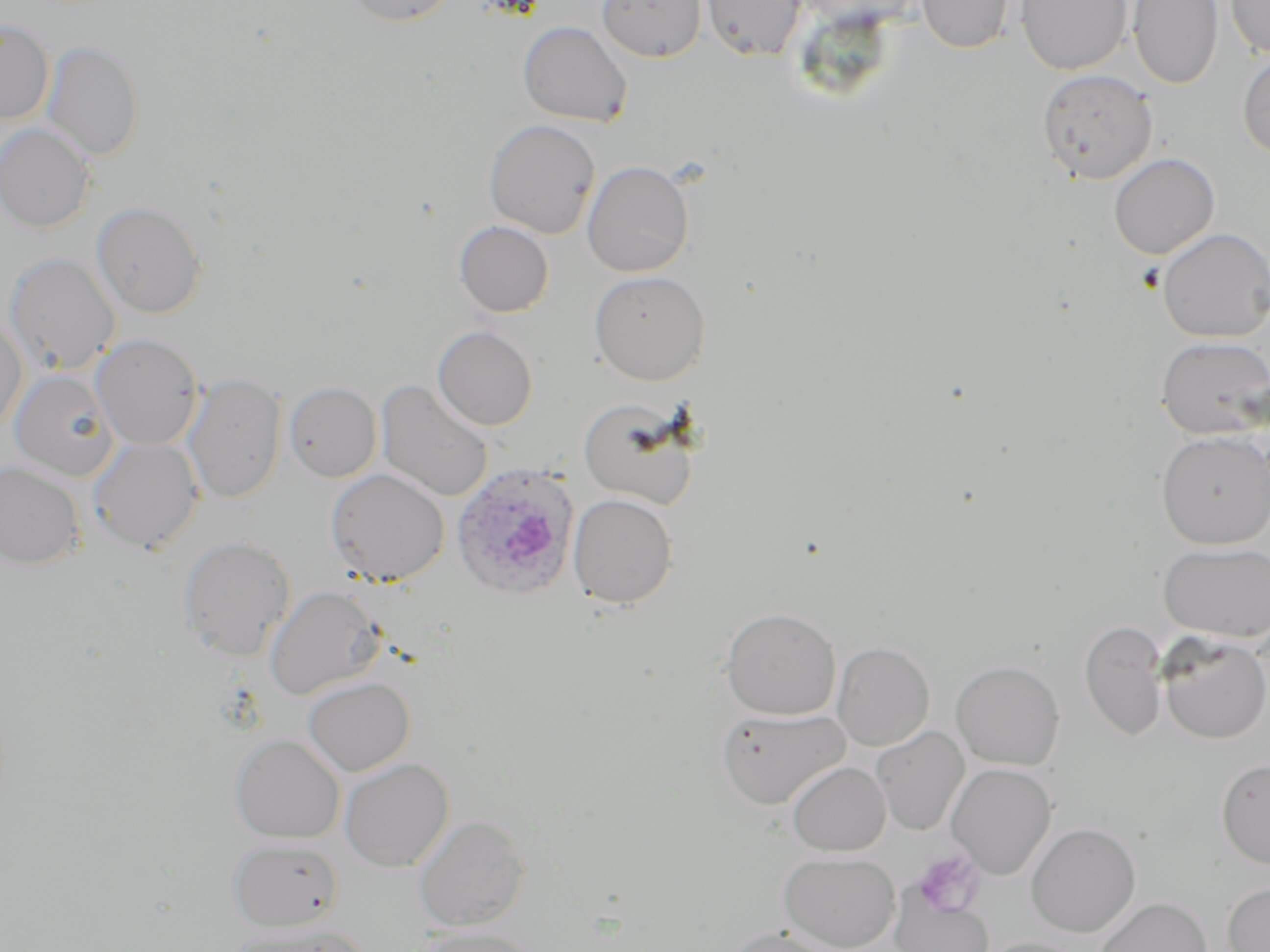

slide-level diagnosis = Plasmodium ovale
image size = 1270×952 pixels
preparation = thin blood smear
stain = May-Grünwald-Giemsa
modality = light microscopy
magnification = 1000x
Plasmodium ovale-infected red blood cell locations = approximate bounding boxes as (x1, y1, x2, y2) in pixels: (451, 463, 580, 599)
platelet locations = approximate bounding boxes as (x1, y1, x2, y2) in pixels: (912, 849, 985, 918)
uninfected red blood cell locations = approximate bounding boxes as (x1, y1, x2, y2) in pixels: (341, 0, 460, 26), (597, 0, 708, 63), (700, 0, 807, 61), (916, 0, 1015, 53), (1016, 0, 1132, 75), (1128, 0, 1223, 89), (1225, 0, 1270, 60), (0, 17, 54, 125), (518, 20, 633, 127), (42, 40, 144, 161), (1237, 50, 1270, 161), (1036, 68, 1158, 184), (483, 119, 600, 239), (0, 123, 95, 233), (1109, 153, 1219, 260), (582, 161, 694, 277), (91, 200, 207, 318), (454, 220, 554, 317), (1157, 227, 1270, 342), (3, 252, 121, 376), (589, 270, 710, 385), (0, 315, 27, 433), (432, 326, 537, 430), (90, 333, 203, 450), (1156, 336, 1270, 440), (8, 369, 119, 481), (181, 372, 286, 504), (375, 379, 494, 502), (283, 381, 382, 482), (579, 397, 700, 510), (1157, 431, 1270, 548), (88, 437, 204, 554), (0, 461, 85, 568), (325, 468, 450, 587), (568, 493, 677, 608), (179, 534, 296, 661), (1158, 541, 1270, 642), (264, 585, 384, 701), (721, 607, 841, 719), (1079, 620, 1168, 741), (1158, 633, 1270, 745), (832, 642, 935, 750), (950, 660, 1064, 770), (302, 676, 415, 777), (716, 706, 849, 809), (870, 726, 970, 835), (230, 734, 345, 843), (339, 757, 454, 872), (1217, 758, 1270, 869), (787, 761, 891, 856), (945, 763, 1056, 879), (413, 814, 530, 931), (1026, 823, 1140, 938), (229, 837, 343, 932), (779, 851, 899, 951), (1222, 882, 1270, 952), (890, 890, 994, 952), (1095, 897, 1212, 952), (229, 919, 369, 952), (416, 924, 542, 951), (724, 925, 843, 952), (981, 938, 1089, 952)
field of view = single